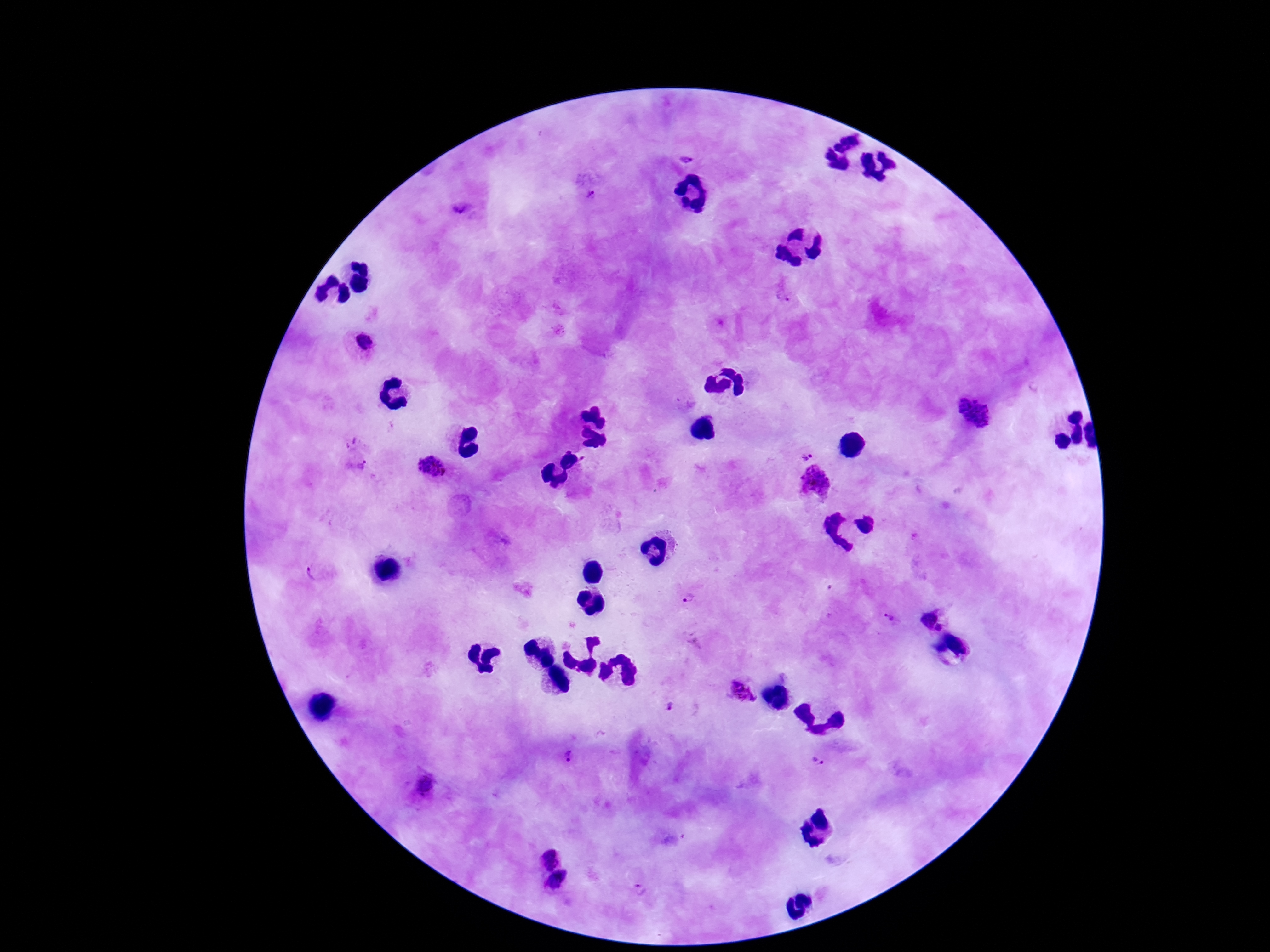
{
  "field_of_view": "one from this slide",
  "stain": "Giemsa",
  "image_size": "1270×952 pixels",
  "patient_malaria_status": "infected",
  "plasmodium_parasite_locations": "approximate centers as (x, y) in pixels: (685, 156), (590, 191), (465, 211), (784, 294), (363, 343), (975, 412), (808, 452), (358, 465), (433, 467), (818, 482), (320, 573), (688, 598), (888, 617), (929, 618), (941, 629), (741, 688), (670, 708), (568, 756), (817, 761), (424, 786), (549, 858), (559, 885), (638, 889)",
  "preparation": "thick blood film",
  "magnification": "100x",
  "capture": "smartphone camera through the microscope eyepiece"
}